Assess this cell for malaria.
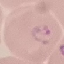

It is parasitized.

{
  "stain": "Giemsa",
  "preparation": "thin smear",
  "capture": "smartphone through the microscope eyepiece",
  "image_type": "automatically extracted cell patch, resized to 64 × 64 pixels"
}